Outline each Plasmodium vivax-infected red blood cell.
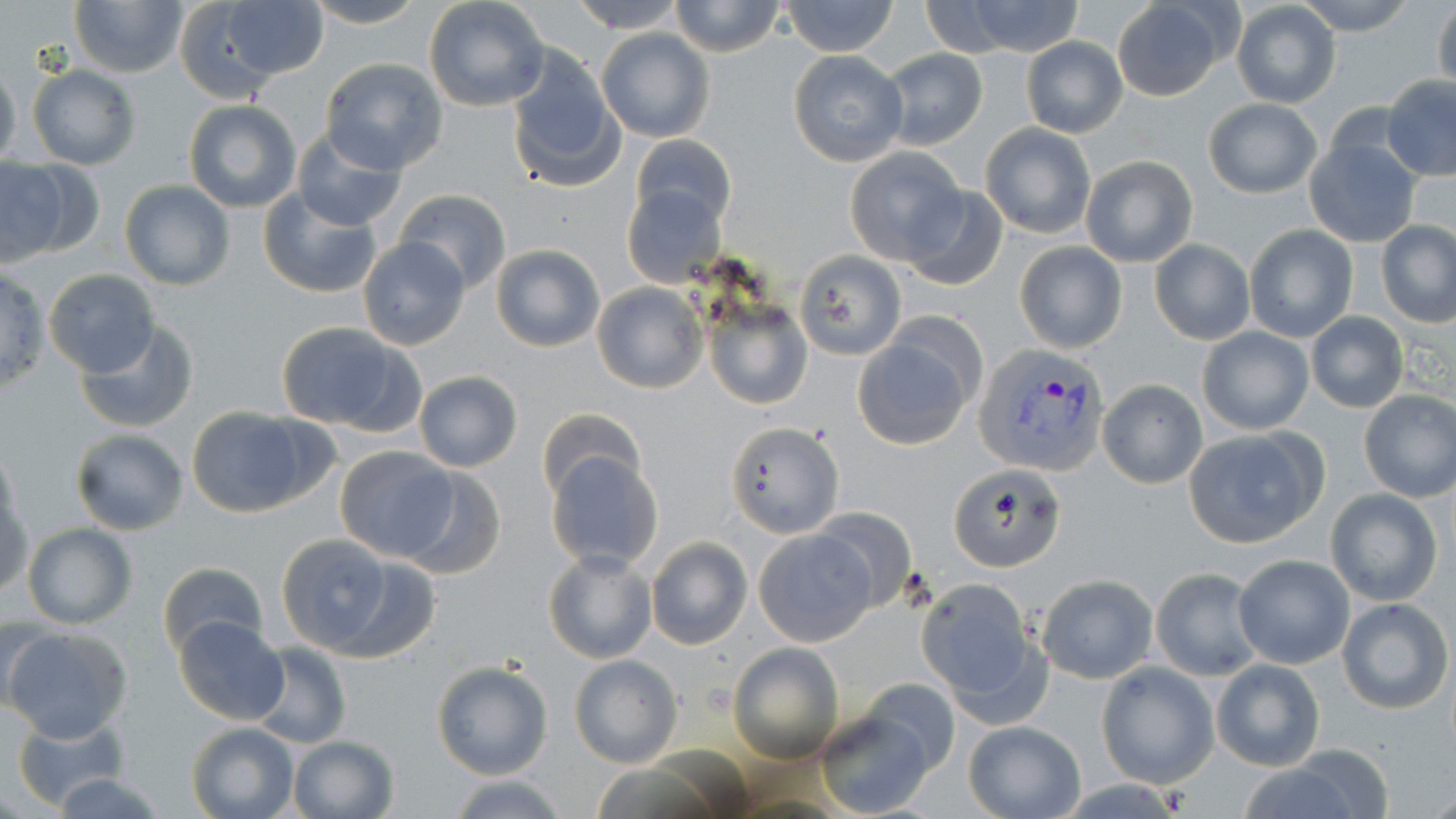
Approximate bounding boxes as (x1, y1, x2, y2) in pixels.
Plasmodium vivax-infected red blood cells: (974, 342, 1110, 474).

slide-level diagnosis = Plasmodium vivax
uninfected red blood cell locations = approximate bounding boxes as (x1, y1, x2, y2) in pixels: (69, 0, 189, 78), (176, 0, 322, 100), (304, 0, 426, 27), (423, 0, 549, 112), (566, 0, 688, 34), (1295, 0, 1417, 36), (1432, 0, 1456, 95), (669, 1, 786, 56), (780, 1, 900, 56), (1111, 1, 1232, 100), (1231, 1, 1340, 109), (931, 2, 1087, 57), (596, 29, 715, 142), (1020, 37, 1127, 137), (879, 48, 988, 150), (506, 49, 624, 193), (786, 49, 909, 166), (319, 57, 448, 173), (0, 60, 21, 172), (27, 65, 141, 169), (1381, 75, 1456, 181), (1203, 98, 1322, 198), (183, 100, 302, 212), (980, 123, 1098, 239), (293, 128, 409, 230), (629, 133, 737, 232), (1304, 137, 1422, 246), (844, 147, 965, 264), (1080, 156, 1197, 267), (0, 157, 94, 265), (119, 180, 234, 290), (622, 182, 726, 287), (901, 184, 1008, 291), (256, 187, 383, 300), (395, 189, 510, 294), (1376, 220, 1456, 326), (1244, 224, 1357, 343), (356, 237, 471, 352), (1150, 239, 1254, 344), (1014, 241, 1127, 353), (490, 243, 606, 351), (796, 251, 904, 360), (0, 266, 50, 394), (45, 269, 161, 378), (591, 282, 707, 394), (701, 291, 812, 411), (1306, 312, 1409, 412), (73, 320, 200, 434), (275, 321, 413, 432), (1198, 325, 1314, 436), (853, 330, 980, 449), (413, 370, 522, 472), (1096, 379, 1207, 488), (1358, 389, 1456, 502), (185, 405, 320, 518), (538, 407, 646, 504), (725, 419, 843, 538), (1182, 427, 1325, 548), (69, 428, 189, 535), (0, 445, 24, 546), (334, 445, 457, 560), (545, 448, 664, 573), (397, 464, 505, 580), (950, 464, 1066, 572), (0, 488, 33, 600), (1325, 488, 1444, 607), (808, 506, 918, 615), (21, 522, 137, 629), (753, 528, 877, 646), (269, 531, 422, 660), (646, 536, 752, 650), (544, 548, 656, 664), (1233, 554, 1355, 670), (157, 561, 268, 661), (1150, 567, 1264, 681), (1036, 573, 1158, 684), (916, 579, 1043, 711), (1336, 598, 1452, 715), (172, 616, 288, 725), (3, 625, 131, 742), (729, 642, 844, 764), (251, 643, 351, 748), (568, 654, 683, 768), (1211, 658, 1325, 770), (431, 661, 552, 780), (1095, 662, 1217, 789), (860, 677, 961, 776), (811, 707, 934, 819), (10, 712, 134, 811), (962, 719, 1086, 818), (186, 721, 301, 819), (288, 734, 399, 818), (1242, 748, 1392, 819), (445, 772, 569, 818)
magnification = 1000x
field of view = single
modality = light microscopy
stain = May-Grünwald-Giemsa
image size = 1456×819 pixels
preparation = thin blood film